Report the malaria status of this cell.
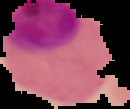
It is parasitized.

From a thin blood film. Image is 130×109 pixels. Segmented cell region on a black background.